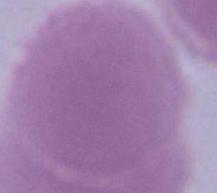
Summary:
  - Identification: red blood cell
  - Modality: photomicrograph
  - Magnification: 1000x